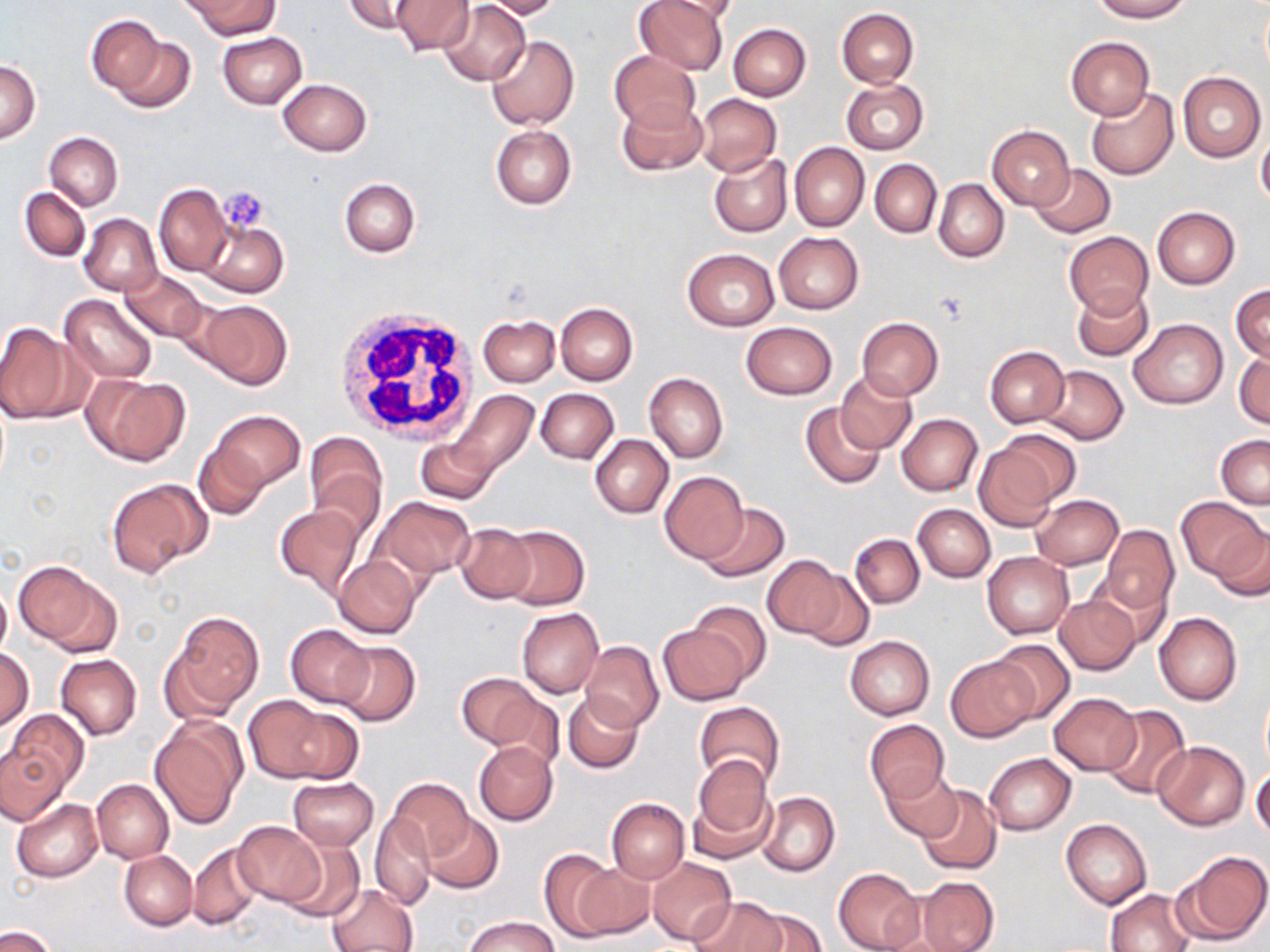
Approximate bounding boxes as (x1,y1)-(x2,y2) corner pairs in pixels. Uninfected red blood cell locations: (344,0)-(426,37), (391,0)-(474,55), (481,0)-(563,19), (633,0)-(730,75), (654,0)-(739,23), (1091,0)-(1191,22), (185,1)-(277,39), (438,1)-(531,85), (836,7)-(919,87), (85,15)-(169,100), (727,22)-(811,100), (217,31)-(307,109), (105,33)-(196,114), (487,35)-(579,130), (1066,37)-(1153,118), (609,49)-(701,133), (2,61)-(39,142), (1177,71)-(1266,162), (277,78)-(372,156), (841,79)-(928,154), (1085,87)-(1179,180), (695,93)-(782,177), (616,97)-(708,176), (490,124)-(577,209), (987,125)-(1076,211), (1257,129)-(1270,208), (44,132)-(123,210), (789,142)-(869,231), (708,152)-(791,237), (870,159)-(941,237), (1030,164)-(1116,239), (869,171)-(1006,251), (934,178)-(1009,262), (339,179)-(419,257), (154,183)-(232,277), (19,187)-(90,262), (1152,207)-(1240,289), (79,213)-(162,296), (200,220)-(288,298), (1064,231)-(1154,317), (774,232)-(863,314), (682,247)-(779,330), (119,268)-(207,341), (1231,284)-(1269,364), (1072,286)-(1154,362), (60,294)-(156,383), (193,298)-(293,389), (555,302)-(638,384), (478,314)-(559,386), (857,318)-(944,401), (1129,319)-(1228,409), (0,321)-(83,425), (741,321)-(836,400), (986,345)-(1069,428), (1234,350)-(1270,429), (1038,365)-(1129,445), (835,370)-(916,453), (645,372)-(727,463), (84,373)-(188,466), (535,388)-(619,464), (448,389)-(540,480), (800,401)-(886,489), (209,410)-(305,491), (897,413)-(982,496), (981,431)-(1077,522), (303,433)-(386,528), (590,434)-(673,519), (1216,434)-(1270,508), (416,436)-(496,503), (192,440)-(269,521), (659,470)-(748,564), (107,479)-(210,577), (1030,495)-(1123,570), (371,496)-(474,582), (1178,497)-(1267,583), (697,500)-(790,582), (914,503)-(995,582), (274,505)-(365,598), (1204,521)-(1270,601), (454,522)-(538,605), (496,525)-(590,610), (1099,526)-(1179,618), (850,533)-(923,609), (982,552)-(1073,638), (762,555)-(860,645), (333,556)-(421,638), (14,561)-(119,654), (0,585)-(11,657), (1055,593)-(1143,675), (682,600)-(773,686), (516,607)-(603,699), (166,612)-(264,715), (1153,612)-(1243,705), (658,623)-(752,706), (285,625)-(374,706), (845,635)-(934,720), (988,639)-(1076,724), (580,640)-(663,732), (332,642)-(421,725), (2,647)-(34,731), (56,653)-(142,738), (946,656)-(1039,742), (456,672)-(548,754), (484,686)-(566,772), (563,691)-(642,773), (1048,692)-(1142,775), (241,694)-(341,783), (693,701)-(786,792), (1103,704)-(1190,799), (4,709)-(88,796), (150,716)-(247,828), (865,719)-(950,805), (1152,740)-(1250,830), (473,741)-(558,825), (0,746)-(68,824), (984,752)-(1076,834), (688,756)-(779,862), (879,766)-(961,840), (1252,768)-(1270,840), (288,777)-(379,850), (389,778)-(474,864), (91,779)-(174,863), (917,784)-(1002,876), (756,791)-(839,877), (606,797)-(690,883), (12,798)-(104,881), (370,811)-(437,911), (422,812)-(503,894), (1061,817)-(1153,909), (231,819)-(327,906), (278,838)-(365,921), (187,842)-(263,931), (119,850)-(197,930), (540,851)-(619,941), (1175,851)-(1270,946), (293,852)-(395,938), (646,856)-(737,946), (569,859)-(654,940), (832,867)-(924,952), (913,876)-(998,951), (327,883)-(418,952), (1106,889)-(1194,952), (691,897)-(785,952), (743,904)-(827,952), (465,916)-(558,952), (1,927)-(55,952). Platelet locations: (218,188)-(269,233), (936,290)-(971,325). White blood cell locations: (331,305)-(479,444). Slide-level diagnosis: negative for blood parasites. May-Grünwald-Giemsa-stained preparation. One field of a larger specimen. Captured at 1000x magnification. Thin blood film. Optical microscopy. Image is 1270×952 pixels.